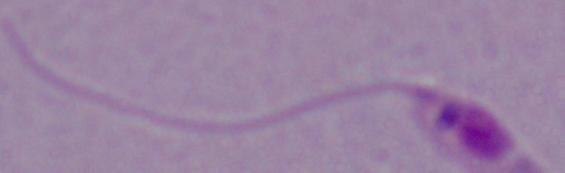
Micrograph. Captured at 1000x magnification. A Leishmania parasite is shown.